Classify this cell by malaria status.
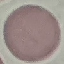
It is uninfected.

Summary:
  - Preparation: thin blood film
  - Image type: cell patch, automatically extracted from a larger field of view and resized to 64 × 64 pixels
  - Stain: Giemsa
  - Capture: smartphone through the microscope eyepiece